Assess this cell for malaria.
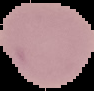
It is uninfected.

Summary:
  - Preparation: thin blood smear
  - Image size: 94×91 pixels
  - Image type: segmented cell region on a black background